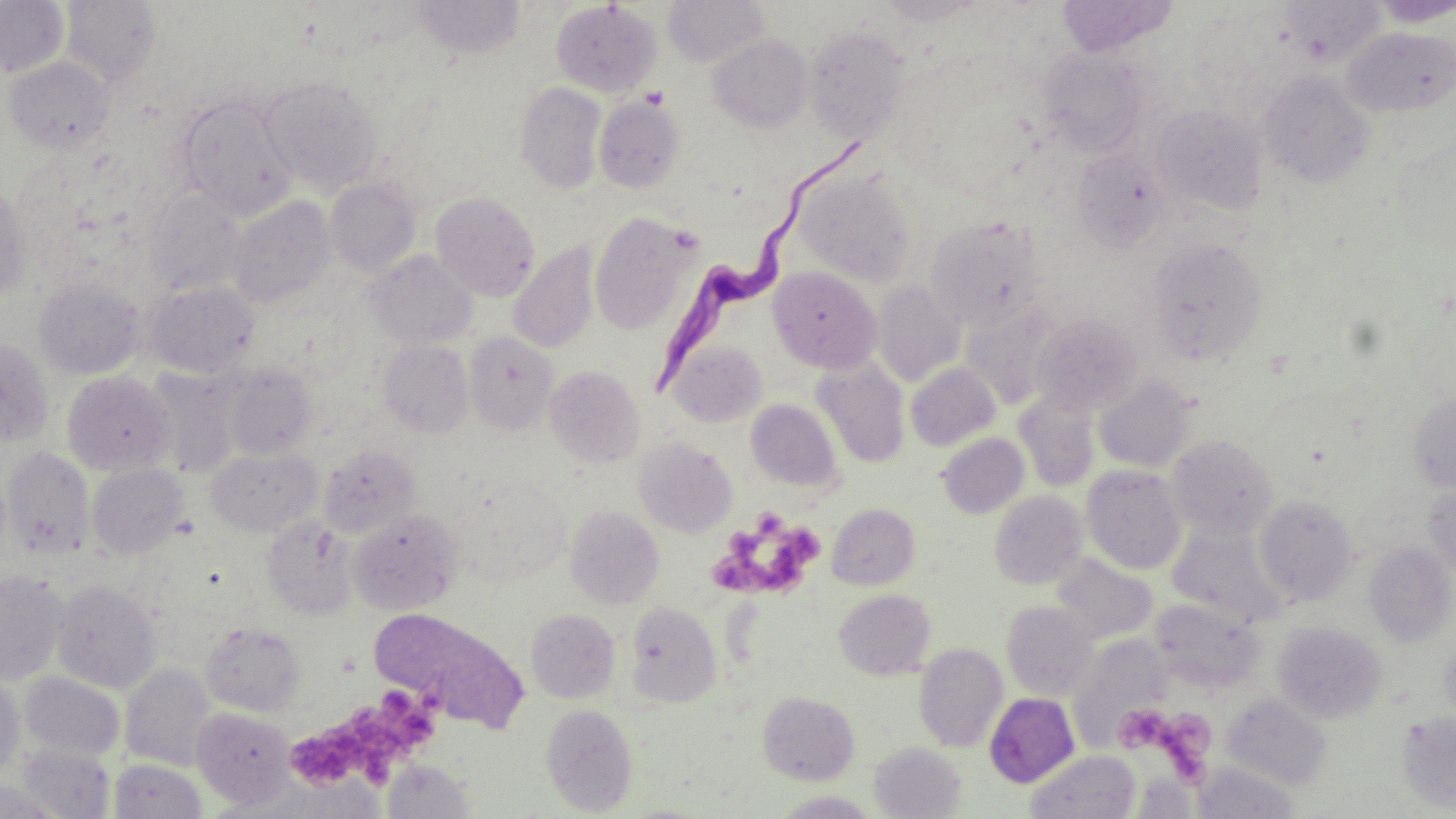

Summary:
  - Coordinate format: approximate bounding boxes as [x1, y1, x2, y2] in pixels
  - Trypanosoma brucei locations: [650, 136, 867, 393]
  - Uninfected red blood cell locations: [412, 0, 525, 60], [664, 0, 770, 67], [877, 0, 985, 25], [1281, 0, 1385, 65], [0, 1, 70, 78], [61, 1, 161, 87], [551, 1, 661, 98], [1056, 1, 1178, 56], [1369, 1, 1456, 27], [804, 25, 911, 143], [1342, 26, 1456, 117], [707, 34, 813, 133], [1040, 48, 1148, 155], [5, 56, 114, 153], [1257, 70, 1374, 188], [260, 75, 382, 194], [516, 82, 606, 193], [176, 92, 298, 219], [594, 96, 684, 193], [1152, 103, 1267, 214], [1389, 134, 1456, 257], [1072, 148, 1171, 251], [793, 168, 916, 286], [326, 177, 421, 276], [0, 182, 32, 301], [144, 190, 245, 296], [431, 191, 540, 301], [228, 196, 336, 308], [589, 212, 701, 334], [925, 215, 1046, 331], [1146, 237, 1268, 365], [509, 242, 600, 354], [367, 250, 477, 347], [768, 266, 882, 373], [33, 277, 145, 380], [872, 281, 966, 386], [146, 282, 259, 377], [960, 302, 1065, 409], [1029, 313, 1143, 417], [464, 331, 558, 435], [0, 338, 54, 446], [378, 339, 474, 438], [668, 340, 768, 427], [812, 359, 910, 468], [224, 362, 318, 459], [905, 363, 1001, 451], [545, 365, 645, 468], [147, 368, 243, 477], [62, 371, 176, 476], [1094, 374, 1198, 472], [1012, 391, 1100, 492], [1409, 391, 1456, 493], [746, 399, 843, 492], [937, 432, 1029, 518], [1166, 434, 1278, 539], [634, 437, 738, 537], [317, 445, 421, 539], [2, 447, 95, 559], [206, 447, 323, 536], [87, 463, 188, 557], [1081, 465, 1186, 574], [1423, 480, 1456, 579], [989, 491, 1088, 589], [1254, 494, 1359, 605], [827, 503, 920, 590], [565, 507, 664, 609], [347, 509, 463, 616], [261, 516, 359, 619], [1168, 522, 1288, 628], [1364, 540, 1455, 647], [1053, 553, 1158, 644], [0, 569, 69, 685], [52, 579, 160, 693], [834, 589, 936, 680], [1002, 600, 1098, 701], [625, 601, 722, 707], [1157, 605, 1260, 694], [371, 608, 529, 728], [526, 609, 621, 703], [1273, 621, 1388, 724], [201, 623, 306, 715], [1071, 633, 1169, 749], [915, 642, 1008, 752], [120, 664, 218, 771], [20, 673, 125, 761], [0, 675, 25, 777], [757, 691, 860, 784], [983, 692, 1080, 787], [1222, 693, 1333, 790], [541, 702, 639, 816], [191, 707, 294, 808], [1397, 711, 1456, 813], [869, 741, 966, 818], [17, 743, 114, 818], [1027, 750, 1140, 819], [109, 758, 206, 818], [381, 760, 474, 817], [0, 779, 65, 819], [770, 791, 883, 818]
  - Platelet locations: [713, 507, 822, 601], [353, 680, 445, 784], [1119, 704, 1209, 788], [284, 729, 359, 789]
  - Slide-level diagnosis: Trypanosoma brucei
  - Stain: May-Grünwald-Giemsa
  - Magnification: 1000x
  - Modality: light microscopy
  - Preparation: thin blood film
  - Field of view: single
  - Image size: 1456×819 pixels